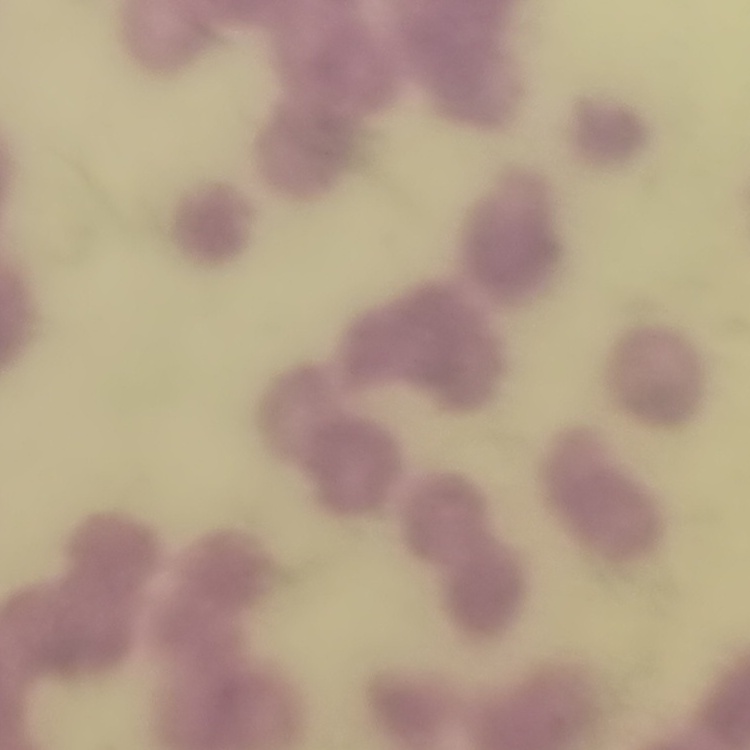

Summary:
  - Erythrocyte morphology: rouleaux formation
  - Preparation: thin blood film
  - Stain: Field's or Giemsa
  - Image type: square crop of a larger photomicrograph